Identify the parasite.
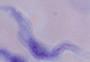
A trypanosome.

Summary:
  - Magnification: 1000x
  - Modality: photomicrograph